Name the cell type shown.
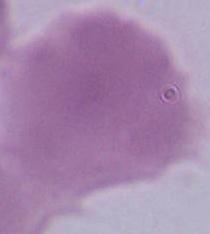
An erythrocyte.

Photomicrograph. 1000x magnification.